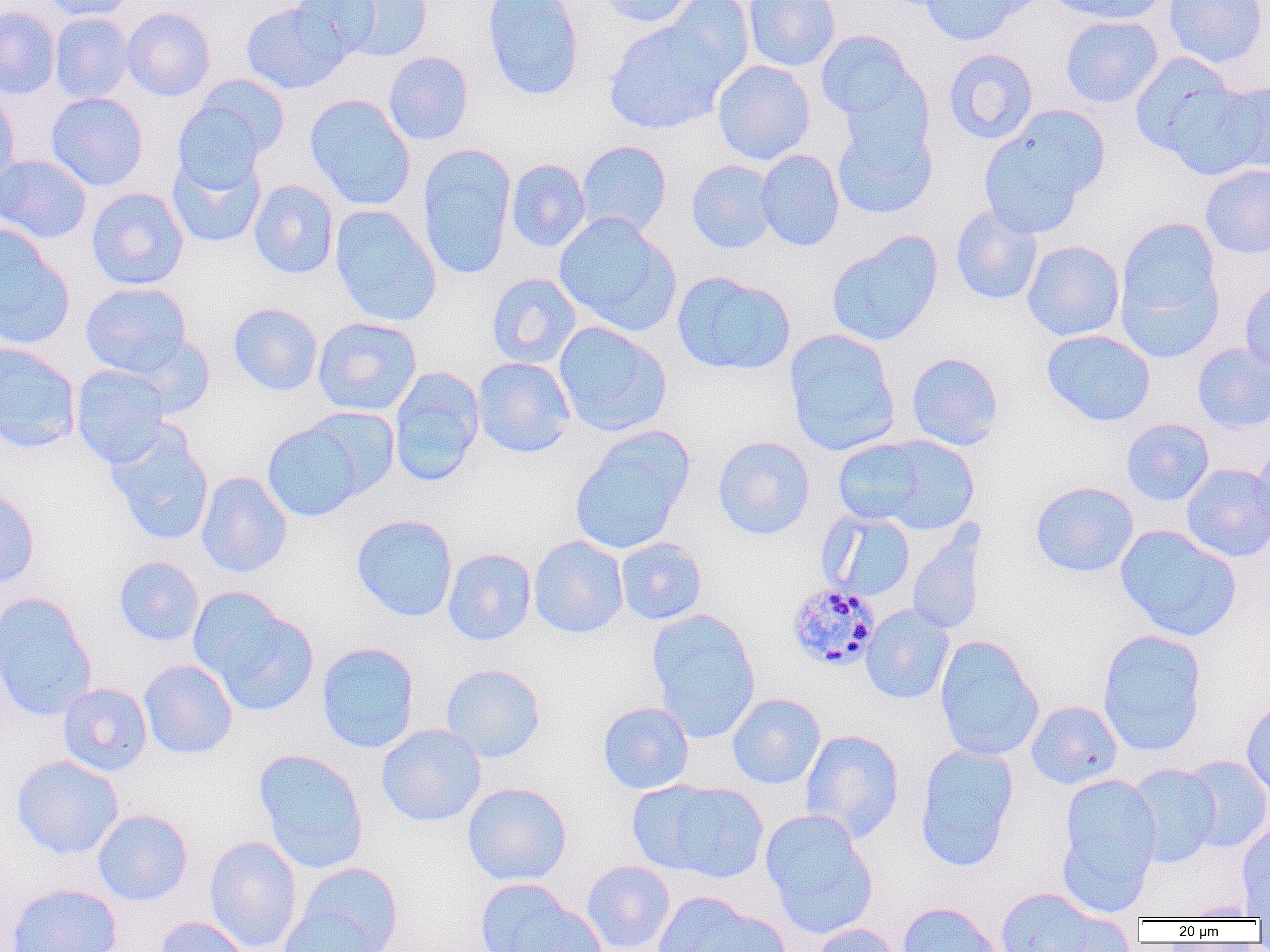
Approximate bounding boxes as [x1, y1, x2, y2] in pixels. Uninfected red blood cell locations: [37, 0, 138, 22], [291, 0, 384, 57], [482, 0, 585, 101], [593, 0, 700, 27], [663, 0, 754, 88], [743, 0, 841, 72], [918, 0, 1029, 47], [1046, 0, 1167, 24], [1164, 0, 1268, 68], [240, 1, 351, 94], [337, 1, 433, 62], [0, 6, 61, 101], [121, 6, 215, 101], [49, 12, 134, 104], [1059, 15, 1164, 109], [603, 19, 734, 135], [815, 29, 922, 127], [942, 48, 1038, 145], [383, 51, 474, 145], [1130, 52, 1243, 162], [712, 60, 816, 165], [183, 75, 291, 168], [1162, 79, 1269, 182], [0, 90, 20, 194], [45, 92, 148, 191], [305, 94, 416, 210], [172, 100, 269, 193], [978, 109, 1107, 238], [831, 114, 938, 220], [576, 140, 672, 238], [417, 145, 516, 280], [755, 149, 845, 252], [166, 150, 266, 249], [0, 153, 92, 244], [505, 159, 591, 252], [686, 159, 778, 254], [1200, 164, 1270, 259], [248, 179, 339, 280], [86, 187, 189, 290], [329, 204, 441, 327], [950, 205, 1043, 306], [553, 212, 682, 337], [1114, 217, 1225, 357], [0, 226, 74, 350], [825, 231, 944, 348], [1022, 240, 1125, 341], [672, 270, 796, 376], [486, 273, 580, 369], [1239, 276, 1270, 377], [80, 282, 192, 378], [227, 303, 323, 396], [313, 317, 422, 416], [552, 321, 672, 436], [783, 329, 901, 456], [1041, 329, 1156, 426], [124, 332, 216, 419], [0, 342, 81, 453], [1192, 343, 1270, 433], [906, 352, 1004, 451], [472, 357, 576, 458], [70, 365, 170, 469], [388, 366, 485, 487], [297, 406, 400, 501], [1121, 418, 1214, 506], [261, 420, 369, 522], [106, 425, 214, 546], [569, 427, 695, 556], [867, 434, 980, 535], [712, 436, 815, 540], [832, 437, 934, 527], [1251, 442, 1270, 542], [1180, 463, 1270, 562], [196, 471, 293, 578], [1030, 481, 1139, 577], [0, 487, 40, 590], [819, 511, 916, 602], [351, 514, 458, 622], [1114, 524, 1242, 642], [907, 525, 988, 636], [529, 535, 629, 639], [615, 537, 707, 625], [442, 548, 537, 646], [114, 556, 204, 646], [190, 590, 318, 716], [0, 593, 97, 722], [861, 605, 954, 705], [645, 608, 761, 740], [1096, 629, 1207, 756], [933, 634, 1045, 761], [316, 642, 420, 754], [139, 659, 238, 759], [440, 663, 546, 763], [57, 682, 153, 777], [726, 692, 826, 789], [1026, 700, 1123, 790], [1240, 700, 1270, 803], [597, 701, 694, 794], [376, 723, 486, 827], [800, 728, 904, 843], [914, 743, 1019, 872], [253, 748, 369, 874], [11, 754, 124, 860], [1180, 755, 1270, 853], [1125, 763, 1221, 867], [1056, 773, 1162, 914], [632, 779, 769, 884], [462, 782, 572, 886], [92, 809, 193, 906], [760, 809, 878, 939], [1235, 822, 1270, 919], [203, 835, 302, 952], [581, 860, 675, 952], [291, 861, 404, 952], [474, 877, 600, 952], [4, 882, 122, 952], [992, 885, 1115, 951], [652, 892, 787, 952], [1177, 901, 1264, 920], [897, 902, 1005, 952], [276, 905, 387, 952], [154, 916, 252, 952], [808, 922, 904, 952]. Plasmodium malariae-infected red blood cell locations: [786, 582, 881, 672]. Slide-level diagnosis: Plasmodium malariae. One field of a larger specimen. Image is 1270×952 pixels. Light microscopy. Captured at 1000x magnification. Thin blood film.